State the blood parasite species.
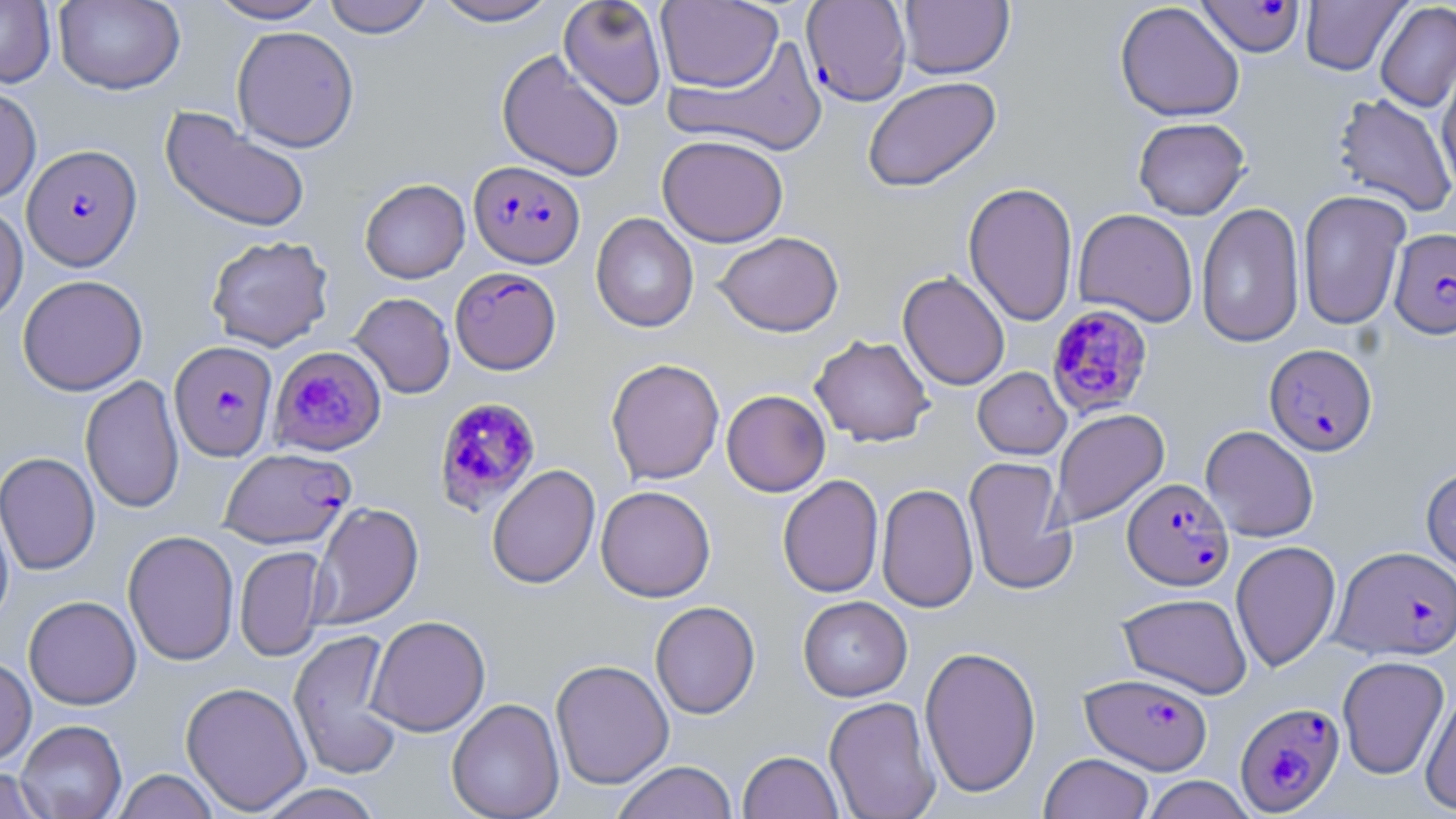

Plasmodium falciparum.

image size = 1456×819 pixels
field of view = one of a larger specimen
Plasmodium falciparum-infected red blood cell locations = approximate bounding boxes as (x1,y1)-(x2,y2) corner pairs in pixels: (1196,0)-(1306,58), (801,1)-(912,106), (22,144)-(142,271), (468,160)-(585,268), (1389,228)-(1456,339), (450,267)-(561,374), (1046,304)-(1154,419), (168,341)-(277,462), (270,344)-(387,456), (1264,344)-(1378,456), (433,396)-(542,516), (219,447)-(355,549), (1123,478)-(1233,591), (1332,546)-(1456,660), (1080,672)-(1213,774), (1234,702)-(1345,815)
uninfected red blood cell locations = approximate bounding boxes as (x1,y1)-(x2,y2) corner pairs in pixels: (0,0)-(55,88), (53,0)-(185,95), (206,0)-(332,24), (322,0)-(434,38), (429,0)-(563,27), (558,0)-(668,110), (898,0)-(1014,79), (1301,0)-(1409,75), (655,1)-(783,92), (1114,1)-(1245,122), (1375,2)-(1456,112), (231,26)-(359,152), (666,36)-(831,156), (497,49)-(625,181), (1437,59)-(1456,195), (862,76)-(1002,193), (0,84)-(41,205), (1332,93)-(1456,217), (161,107)-(311,235), (1133,116)-(1250,219), (657,134)-(789,247), (359,178)-(470,284), (963,181)-(1079,327), (1297,189)-(1410,330), (1196,202)-(1305,348), (0,203)-(28,324), (1073,208)-(1198,327), (591,213)-(699,333), (713,231)-(844,337), (206,235)-(334,351), (897,270)-(1010,390), (17,275)-(148,396), (350,292)-(455,398), (810,335)-(935,447), (606,358)-(725,485), (973,367)-(1071,460), (80,375)-(184,514), (721,390)-(830,497), (1050,408)-(1169,529), (1200,425)-(1319,542), (0,451)-(100,576), (963,456)-(1076,595), (486,464)-(600,589), (1420,464)-(1456,579), (778,474)-(884,598), (876,483)-(979,613), (596,485)-(715,602), (0,494)-(15,629), (309,501)-(424,629), (123,530)-(240,666), (1230,540)-(1341,672), (235,546)-(329,661), (1117,592)-(1252,699), (23,595)-(141,710), (798,595)-(912,701), (650,601)-(760,719), (366,615)-(491,737), (288,629)-(406,781), (919,645)-(1041,798), (1337,655)-(1450,779), (0,656)-(37,766), (550,659)-(674,789), (180,681)-(312,814), (1420,688)-(1456,815), (824,696)-(941,819), (446,698)-(565,819), (15,719)-(127,818), (738,750)-(843,818), (1039,753)-(1155,819), (611,760)-(739,819), (0,766)-(50,819), (112,769)-(219,819), (1140,775)-(1257,818), (254,783)-(385,819)
preparation = thin blood film
magnification = 1000x
modality = light microscopy
stain = May-Grünwald-Giemsa